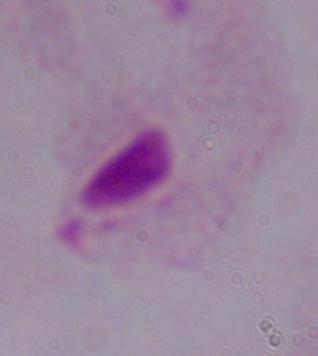
1000x magnification. A trichomonad is seen. Micrograph.